Classify this cell by malaria status.
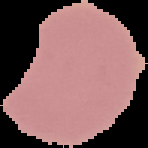

Parasitized.

Image is 148×148 pixels. From a thin blood film. Cell region segmented out of the field of view; the surrounding area is masked to black.